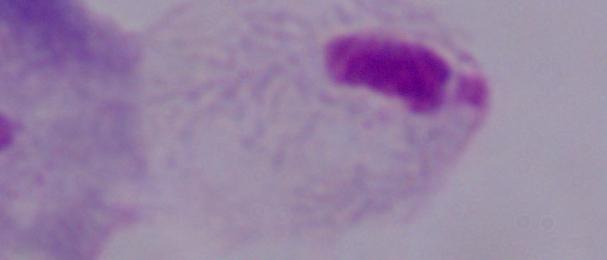

identification = trichomonad
modality = photomicrograph
magnification = 1000x